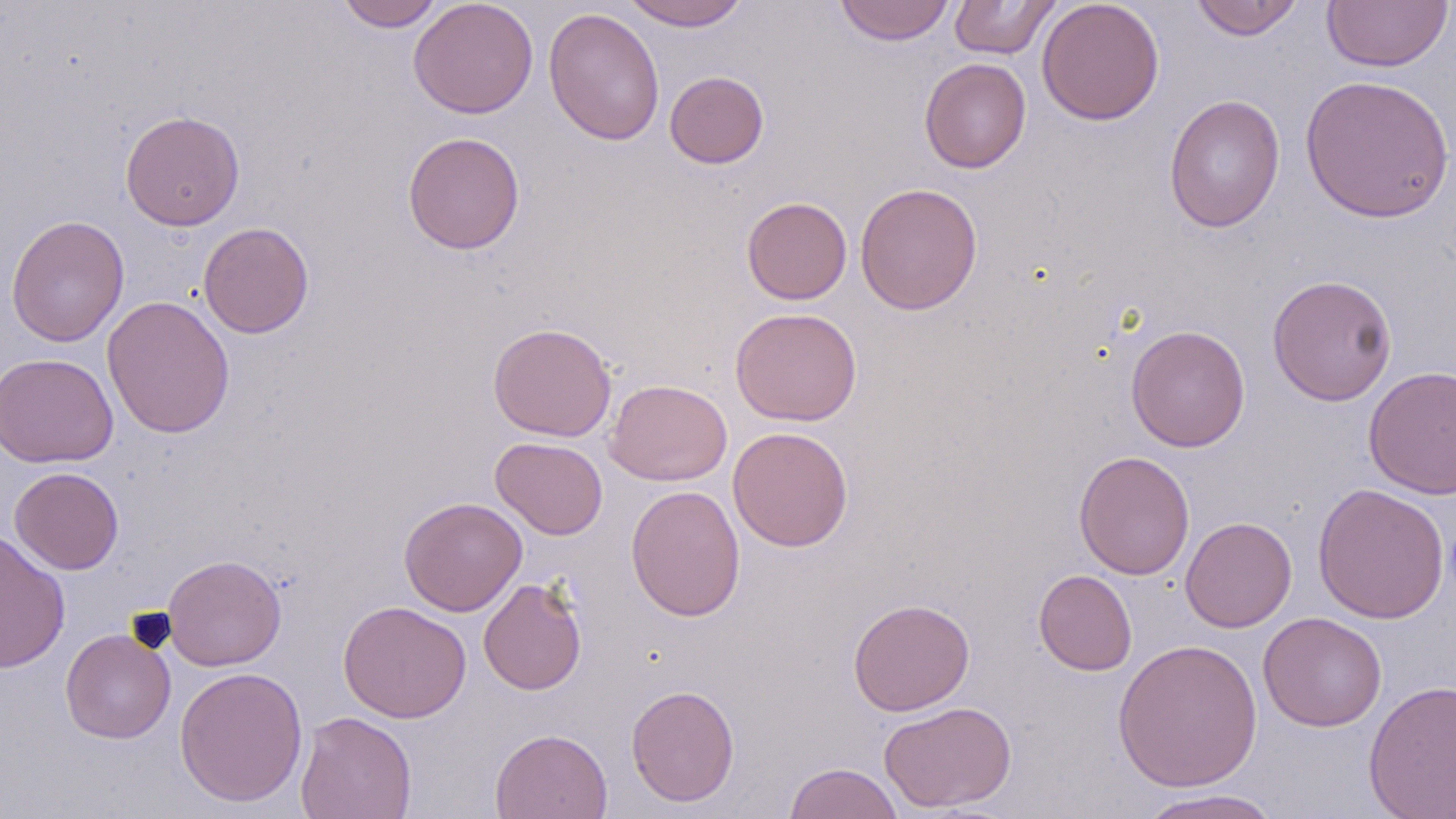
Approximate bounding boxes as [x1, y1, x2, y2] in pixels. Uninfected red blood cell locations: [335, 0, 443, 31], [409, 0, 538, 119], [621, 0, 752, 31], [834, 0, 955, 46], [949, 0, 1061, 59], [1036, 0, 1165, 126], [1188, 0, 1305, 41], [1322, 1, 1453, 72], [543, 7, 665, 145], [919, 57, 1031, 173], [665, 70, 769, 169], [1299, 74, 1455, 224], [1164, 93, 1286, 233], [120, 110, 245, 231], [402, 131, 525, 254], [855, 181, 983, 315], [742, 196, 852, 305], [6, 214, 129, 347], [198, 222, 315, 339], [1266, 274, 1398, 406], [101, 294, 235, 439], [730, 306, 862, 426], [487, 322, 617, 442], [1125, 325, 1250, 452], [0, 352, 118, 468], [1363, 365, 1456, 500], [605, 379, 732, 486], [728, 426, 853, 552], [490, 436, 608, 540], [1074, 450, 1195, 580], [9, 467, 124, 574], [1311, 483, 1451, 624], [626, 485, 746, 621], [399, 497, 526, 616], [1180, 516, 1297, 633], [0, 529, 71, 674], [162, 554, 286, 671], [1033, 569, 1137, 675], [478, 577, 587, 695], [847, 598, 975, 716], [337, 600, 472, 723], [1258, 612, 1387, 732], [60, 628, 175, 744], [1112, 638, 1263, 792], [174, 666, 308, 807], [1363, 679, 1456, 819], [625, 684, 740, 807], [878, 700, 1016, 813], [294, 710, 417, 819], [489, 728, 613, 819], [783, 762, 905, 819], [1131, 789, 1284, 819]. Slide-level diagnosis: no evidence of blood parasites. Thin blood smear. 1000x magnification. One field of a larger specimen. Image is 1456×819 pixels. May-Grünwald-Giemsa stain. Light microscopy.